Describe the morphology of the erythrocytes.
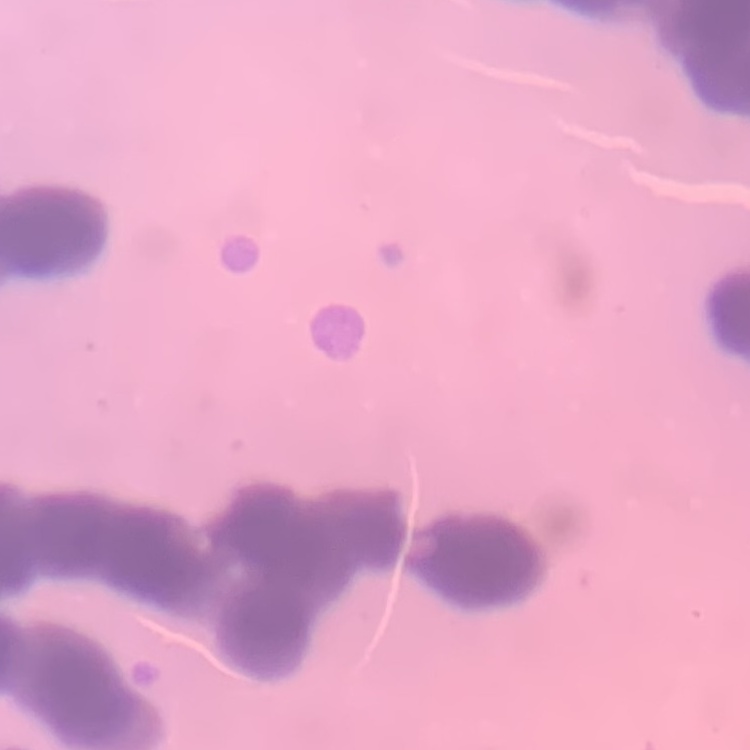

Rouleaux formation.

stain: Field's or Giemsa
image_type: square crop of a larger photomicrograph
preparation: thin blood film